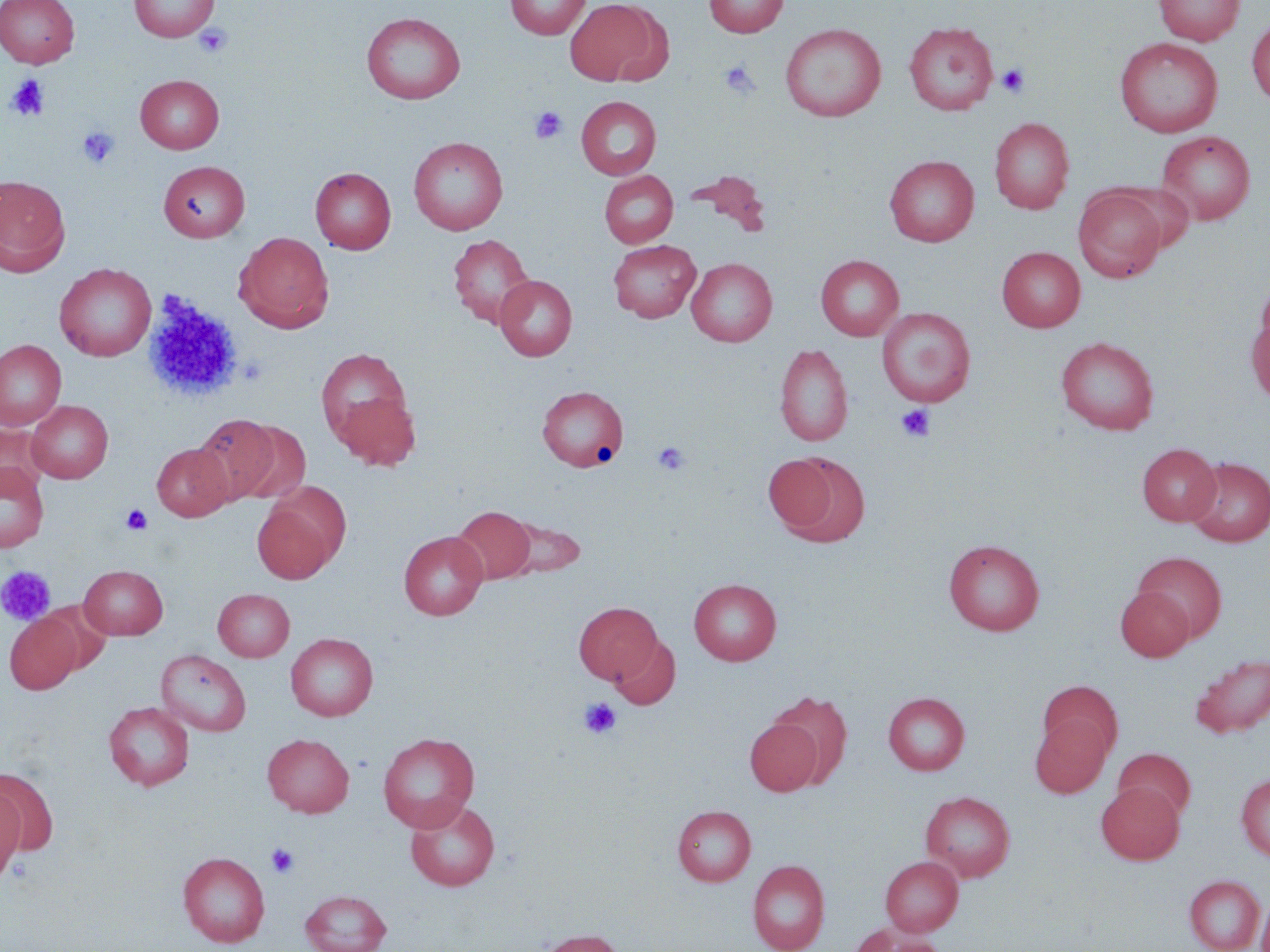 Approximate bounding boxes as (x1, y1, x2, y2) in pixels. Uninfected red blood cell locations: (0, 0, 79, 68), (129, 0, 218, 41), (505, 0, 591, 40), (564, 0, 665, 86), (703, 0, 788, 37), (1154, 0, 1245, 46), (361, 12, 465, 104), (1247, 17, 1270, 105), (903, 21, 998, 115), (780, 23, 886, 122), (1115, 37, 1223, 138), (135, 74, 224, 153), (576, 96, 662, 180), (989, 117, 1075, 214), (1157, 130, 1255, 225), (408, 136, 508, 235), (884, 155, 979, 247), (159, 161, 250, 242), (310, 167, 396, 254), (685, 169, 771, 233), (599, 170, 678, 248), (0, 175, 71, 276), (1112, 182, 1196, 253), (1073, 186, 1167, 282), (234, 232, 334, 332), (448, 234, 535, 328), (608, 240, 701, 322), (996, 247, 1086, 332), (816, 255, 904, 341), (686, 258, 777, 346), (54, 263, 156, 361), (1255, 274, 1270, 357), (495, 275, 577, 360), (876, 307, 976, 407), (1247, 309, 1270, 409), (1055, 336, 1160, 435), (0, 340, 66, 430), (774, 343, 854, 447), (315, 347, 414, 448), (537, 385, 628, 471), (334, 392, 421, 471), (26, 400, 113, 483), (193, 413, 282, 503), (231, 421, 312, 506), (0, 424, 50, 498), (152, 443, 234, 521), (1137, 443, 1221, 526), (772, 452, 871, 547), (1184, 457, 1270, 546), (0, 462, 49, 553), (252, 500, 337, 584), (451, 505, 539, 585), (492, 513, 586, 579), (399, 531, 488, 620), (943, 539, 1044, 635), (1132, 552, 1226, 643), (78, 564, 168, 639), (689, 578, 781, 665), (1115, 586, 1194, 661), (213, 588, 295, 661), (573, 602, 662, 684), (4, 614, 82, 693), (285, 633, 378, 721), (609, 635, 680, 710), (156, 649, 251, 737), (1190, 653, 1270, 738), (1038, 681, 1123, 760), (767, 690, 853, 785), (883, 692, 970, 775), (103, 701, 194, 790), (1030, 716, 1111, 798), (744, 718, 822, 796), (377, 732, 480, 831), (262, 733, 354, 817), (1113, 748, 1195, 821), (1, 769, 59, 856), (1236, 774, 1270, 861), (1096, 782, 1184, 864), (0, 786, 26, 885), (921, 791, 1015, 882), (405, 798, 500, 891), (672, 804, 756, 886), (179, 852, 270, 947), (881, 856, 963, 936), (747, 860, 830, 952), (1184, 874, 1265, 952), (300, 889, 392, 952), (1257, 894, 1270, 952), (854, 927, 943, 952), (536, 929, 625, 952). Platelet locations: (194, 23, 233, 58), (719, 61, 759, 98), (996, 62, 1031, 98), (6, 74, 50, 121), (529, 106, 568, 144), (77, 126, 120, 169), (142, 291, 244, 402), (896, 404, 936, 442), (652, 440, 690, 476), (120, 504, 153, 536), (1, 566, 54, 625), (579, 697, 621, 740), (266, 842, 300, 878). Slide-level diagnosis: no evidence of blood parasites. Thin blood smear. May-Grünwald-Giemsa-stained preparation. Image is 1270×952 pixels. One field of a larger specimen. Optical microscopy. 1000x magnification.